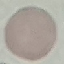

Summary:
  - Malaria status: uninfected
  - Preparation: thin blood smear
  - Image type: automatically extracted cell patch, resized to 64 × 64 pixels
  - Stain: Giemsa
  - Capture: smartphone through the microscope eyepiece